State which parasite is depicted.
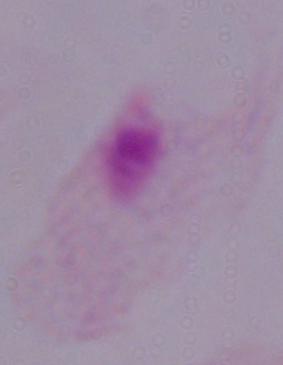
A trichomonad.

Photomicrograph. Captured at 1000x magnification.